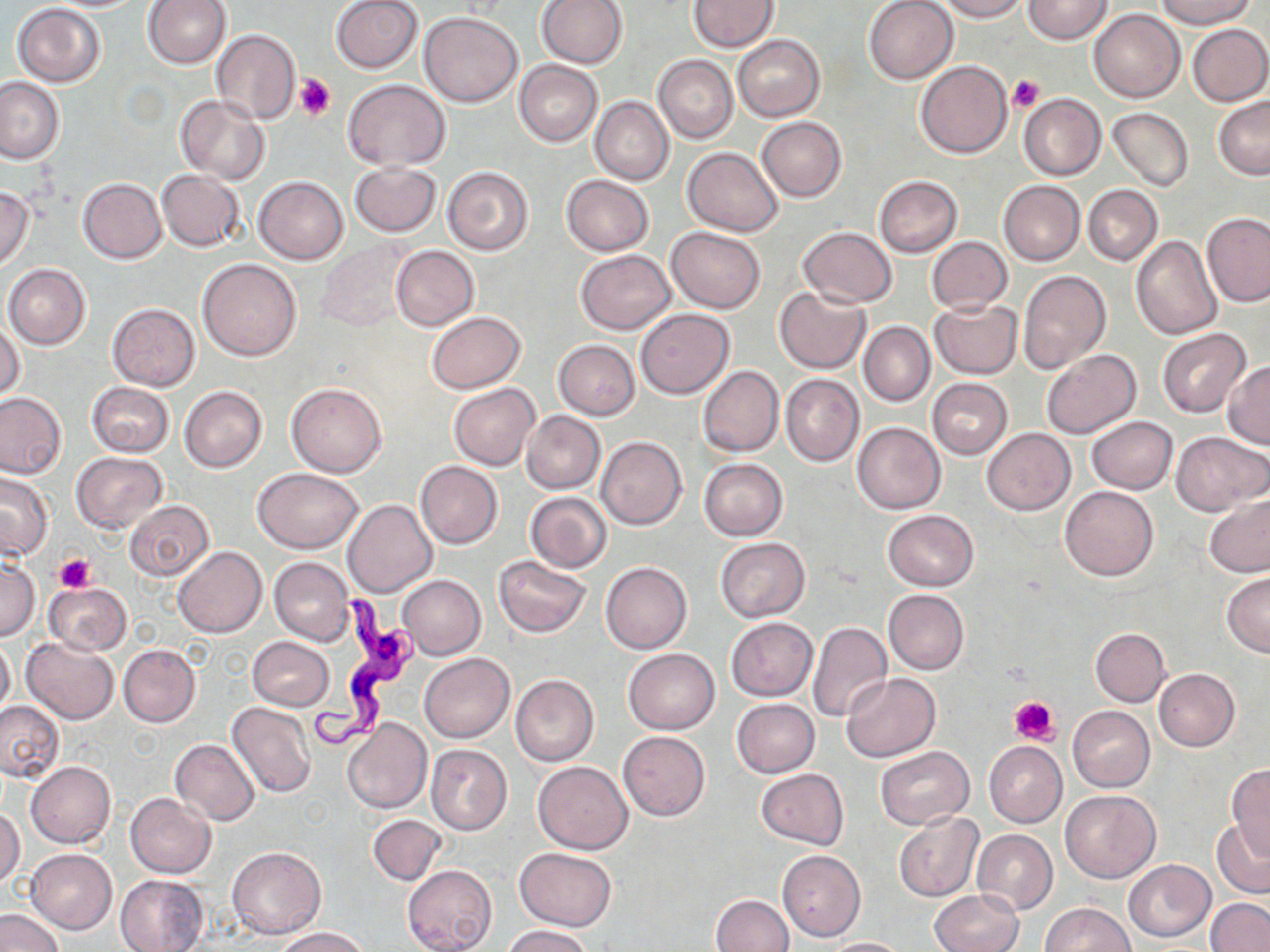
Approximate bounding boxes as [x1, y1, x2, y2] in pixels. Uninfected red blood cell locations: [331, 0, 422, 74], [687, 0, 779, 51], [864, 0, 958, 84], [934, 0, 1027, 21], [1023, 0, 1113, 45], [1156, 0, 1253, 29], [143, 1, 230, 69], [536, 1, 627, 70], [11, 4, 106, 87], [1089, 10, 1185, 102], [419, 11, 522, 107], [1187, 23, 1270, 105], [212, 29, 300, 124], [733, 35, 824, 121], [654, 55, 737, 143], [915, 59, 1011, 158], [514, 60, 603, 146], [0, 76, 66, 164], [342, 79, 451, 170], [1019, 93, 1106, 180], [174, 95, 270, 185], [1213, 95, 1270, 180], [590, 97, 674, 185], [575, 103, 660, 259], [1107, 107, 1193, 192], [756, 116, 846, 202], [682, 146, 784, 237], [347, 162, 440, 237], [441, 166, 534, 255], [156, 170, 244, 251], [561, 175, 654, 255], [873, 176, 962, 256], [254, 177, 348, 263], [77, 178, 167, 263], [998, 180, 1085, 265], [1083, 185, 1162, 266], [0, 187, 34, 270], [1201, 212, 1270, 306], [798, 226, 897, 307], [666, 227, 765, 313], [1129, 235, 1222, 339], [928, 237, 1011, 314], [317, 242, 412, 331], [390, 245, 479, 331], [576, 249, 676, 334], [197, 258, 301, 361], [4, 264, 91, 349], [1017, 270, 1113, 375], [776, 287, 869, 374], [929, 300, 1023, 379], [106, 303, 200, 390], [635, 309, 734, 398], [426, 311, 524, 392], [1, 321, 25, 400], [859, 322, 934, 407], [1157, 329, 1250, 417], [553, 340, 640, 420], [1041, 349, 1140, 438], [1223, 361, 1270, 447], [697, 366, 783, 456], [781, 374, 863, 466], [927, 378, 1012, 458], [87, 382, 174, 456], [287, 382, 386, 478], [449, 384, 540, 469], [178, 386, 267, 472], [0, 392, 69, 479], [522, 410, 605, 494], [1087, 416, 1176, 493], [853, 422, 945, 513], [981, 428, 1074, 516], [1169, 431, 1268, 515], [595, 436, 686, 529], [71, 453, 169, 534], [699, 458, 788, 540], [414, 462, 502, 548], [253, 468, 363, 553], [0, 473, 53, 561], [1059, 486, 1158, 581], [524, 493, 612, 573], [1204, 493, 1270, 578], [342, 499, 436, 597], [122, 501, 215, 581], [883, 509, 978, 590], [716, 538, 810, 622], [172, 547, 266, 637], [1, 555, 40, 641], [494, 556, 591, 637], [269, 557, 354, 645], [600, 561, 692, 654], [1223, 571, 1270, 657], [397, 575, 485, 659], [43, 581, 132, 655], [883, 589, 969, 674], [725, 617, 818, 701], [807, 621, 891, 723], [1091, 628, 1170, 705], [21, 636, 118, 724], [0, 637, 15, 717], [247, 637, 335, 711], [118, 645, 201, 727], [623, 649, 719, 734], [420, 652, 514, 742], [1153, 669, 1240, 752], [840, 673, 939, 761], [511, 674, 600, 766], [732, 699, 819, 777], [0, 700, 65, 783], [228, 701, 317, 798], [1069, 707, 1154, 792], [341, 718, 432, 814], [618, 731, 710, 820], [170, 739, 260, 826], [984, 741, 1066, 826], [424, 744, 511, 836], [876, 746, 974, 829], [25, 761, 115, 849], [532, 761, 633, 853], [1226, 764, 1270, 859], [756, 769, 848, 849], [1059, 790, 1161, 882], [125, 793, 215, 878], [0, 807, 25, 888], [895, 813, 982, 901], [368, 814, 446, 885], [1211, 819, 1270, 896], [972, 829, 1057, 914], [228, 846, 326, 939], [514, 847, 616, 930], [26, 849, 117, 934], [778, 850, 865, 941], [1122, 859, 1216, 941], [402, 864, 496, 951], [115, 874, 209, 952], [931, 890, 1024, 952], [710, 894, 793, 952], [1205, 899, 1270, 952], [1042, 902, 1133, 951], [0, 908, 65, 952], [502, 925, 593, 952], [275, 927, 370, 951], [821, 937, 911, 952]. Platelet locations: [293, 74, 336, 122], [1010, 75, 1044, 112], [53, 553, 94, 596], [1009, 696, 1059, 746]. Trypanosoma brucei locations: [310, 589, 428, 752]. Slide-level diagnosis: Trypanosoma brucei. May-Grünwald-Giemsa-stained preparation. Optical microscopy. Image is 1270×952 pixels. Thin blood film. Captured at 1000x magnification. One field of a larger specimen.